Identify the cell.
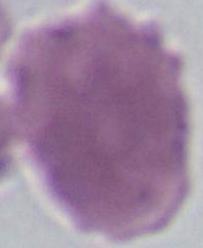
An erythrocyte.

Summary:
  - Magnification: 1000x
  - Modality: photomicrograph